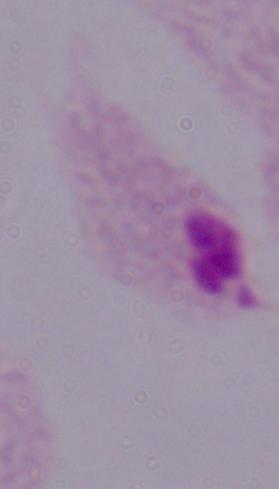

Summary:
  - Magnification: 1000x
  - Identification: trichomonad
  - Modality: photomicrograph